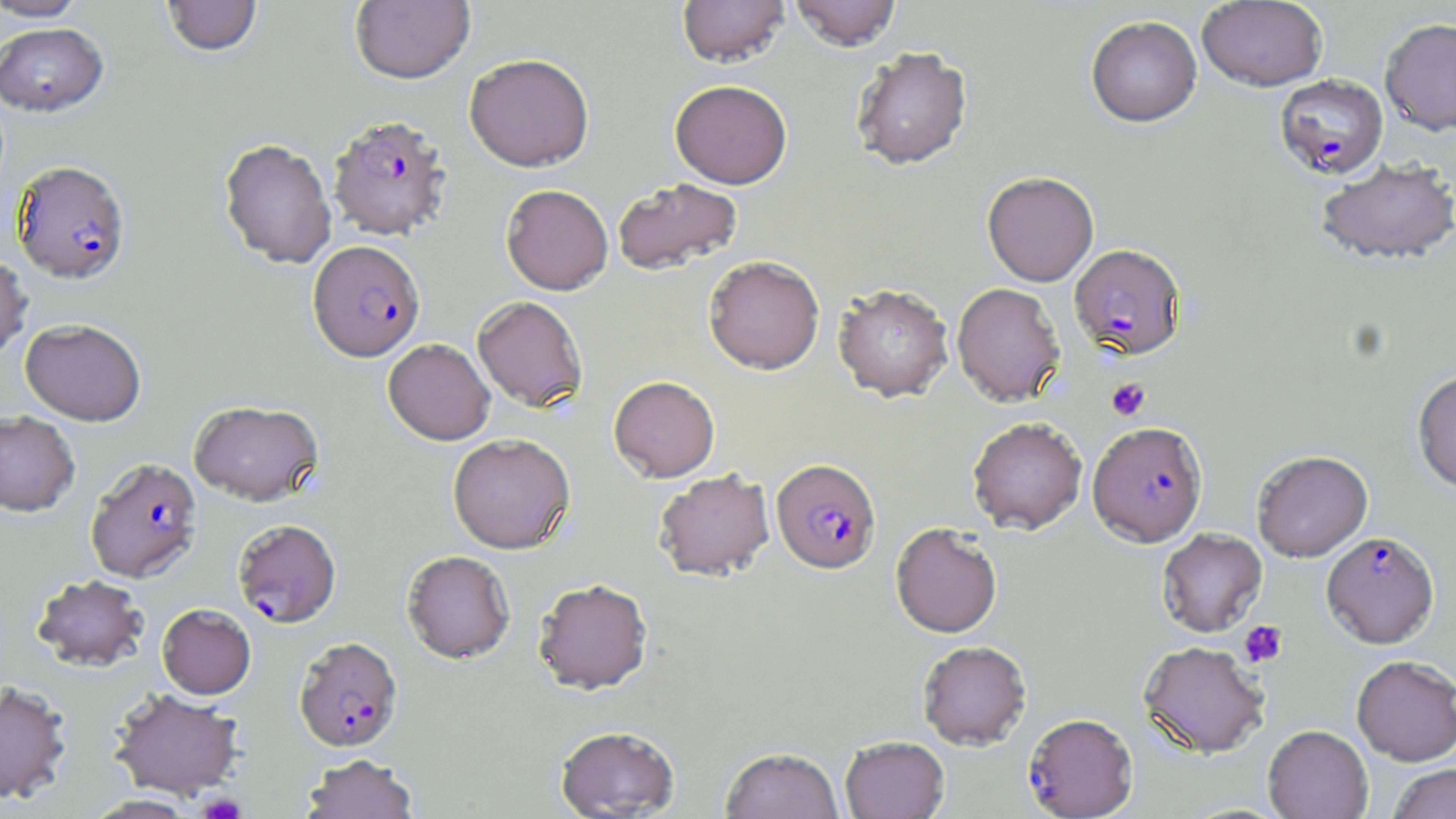

Approximate bounding boxes as named x1/y1/x2/y2 corners in pixels. Platelet locations: (x1=1106, y1=378, x2=1150, y2=421), (x1=1238, y1=620, x2=1288, y2=668), (x1=197, y1=793, x2=245, y2=819). Plasmodium falciparum-infected red blood cell locations: (x1=1274, y1=73, x2=1388, y2=179), (x1=327, y1=114, x2=452, y2=241), (x1=12, y1=160, x2=130, y2=284), (x1=308, y1=240, x2=425, y2=361), (x1=1069, y1=244, x2=1187, y2=360), (x1=1088, y1=421, x2=1207, y2=546), (x1=85, y1=457, x2=203, y2=583), (x1=771, y1=458, x2=881, y2=574), (x1=232, y1=518, x2=341, y2=628), (x1=1321, y1=531, x2=1439, y2=648), (x1=294, y1=637, x2=403, y2=752), (x1=1023, y1=712, x2=1138, y2=818). Uninfected red blood cell locations: (x1=1, y1=0, x2=89, y2=21), (x1=161, y1=0, x2=263, y2=57), (x1=350, y1=0, x2=475, y2=85), (x1=677, y1=0, x2=790, y2=67), (x1=790, y1=0, x2=902, y2=50), (x1=1198, y1=0, x2=1327, y2=91), (x1=1086, y1=15, x2=1202, y2=127), (x1=1380, y1=17, x2=1456, y2=135), (x1=0, y1=22, x2=109, y2=116), (x1=851, y1=46, x2=972, y2=170), (x1=464, y1=53, x2=594, y2=171), (x1=670, y1=79, x2=793, y2=189), (x1=218, y1=138, x2=337, y2=269), (x1=1315, y1=157, x2=1456, y2=266), (x1=982, y1=171, x2=1099, y2=286), (x1=613, y1=177, x2=743, y2=276), (x1=501, y1=184, x2=613, y2=295), (x1=0, y1=251, x2=32, y2=364), (x1=703, y1=255, x2=825, y2=375), (x1=951, y1=282, x2=1066, y2=406), (x1=832, y1=283, x2=954, y2=402), (x1=472, y1=296, x2=588, y2=411), (x1=20, y1=318, x2=146, y2=426), (x1=383, y1=338, x2=495, y2=445), (x1=1412, y1=369, x2=1456, y2=493), (x1=608, y1=375, x2=720, y2=482), (x1=188, y1=400, x2=323, y2=505), (x1=0, y1=410, x2=80, y2=516), (x1=967, y1=416, x2=1087, y2=534), (x1=447, y1=433, x2=575, y2=554), (x1=1252, y1=449, x2=1373, y2=561), (x1=653, y1=470, x2=775, y2=582), (x1=890, y1=522, x2=1002, y2=638), (x1=1156, y1=528, x2=1267, y2=637), (x1=402, y1=550, x2=516, y2=664), (x1=30, y1=574, x2=150, y2=673), (x1=533, y1=578, x2=653, y2=696), (x1=157, y1=604, x2=256, y2=699), (x1=917, y1=640, x2=1032, y2=750), (x1=1138, y1=640, x2=1270, y2=758), (x1=1351, y1=655, x2=1456, y2=765), (x1=0, y1=680, x2=72, y2=804), (x1=109, y1=688, x2=244, y2=799), (x1=555, y1=725, x2=679, y2=818), (x1=1263, y1=725, x2=1373, y2=819), (x1=840, y1=735, x2=949, y2=818), (x1=720, y1=746, x2=844, y2=819), (x1=301, y1=754, x2=419, y2=819), (x1=1387, y1=763, x2=1456, y2=819), (x1=82, y1=794, x2=198, y2=818). Slide-level diagnosis: Plasmodium falciparum. Light microscopy. Single field of view. May-Grünwald-Giemsa-stained preparation. Image is 1456×819 pixels. 1000x magnification. Thin blood film.